Assess this cell for malaria.
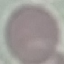

It is uninfected.

{
  "image_type": "cell patch, automatically extracted from a larger field of view and resized to 64 × 64 pixels",
  "stain": "Giemsa",
  "preparation": "thin blood smear",
  "capture": "smartphone camera at the microscope eyepiece"
}